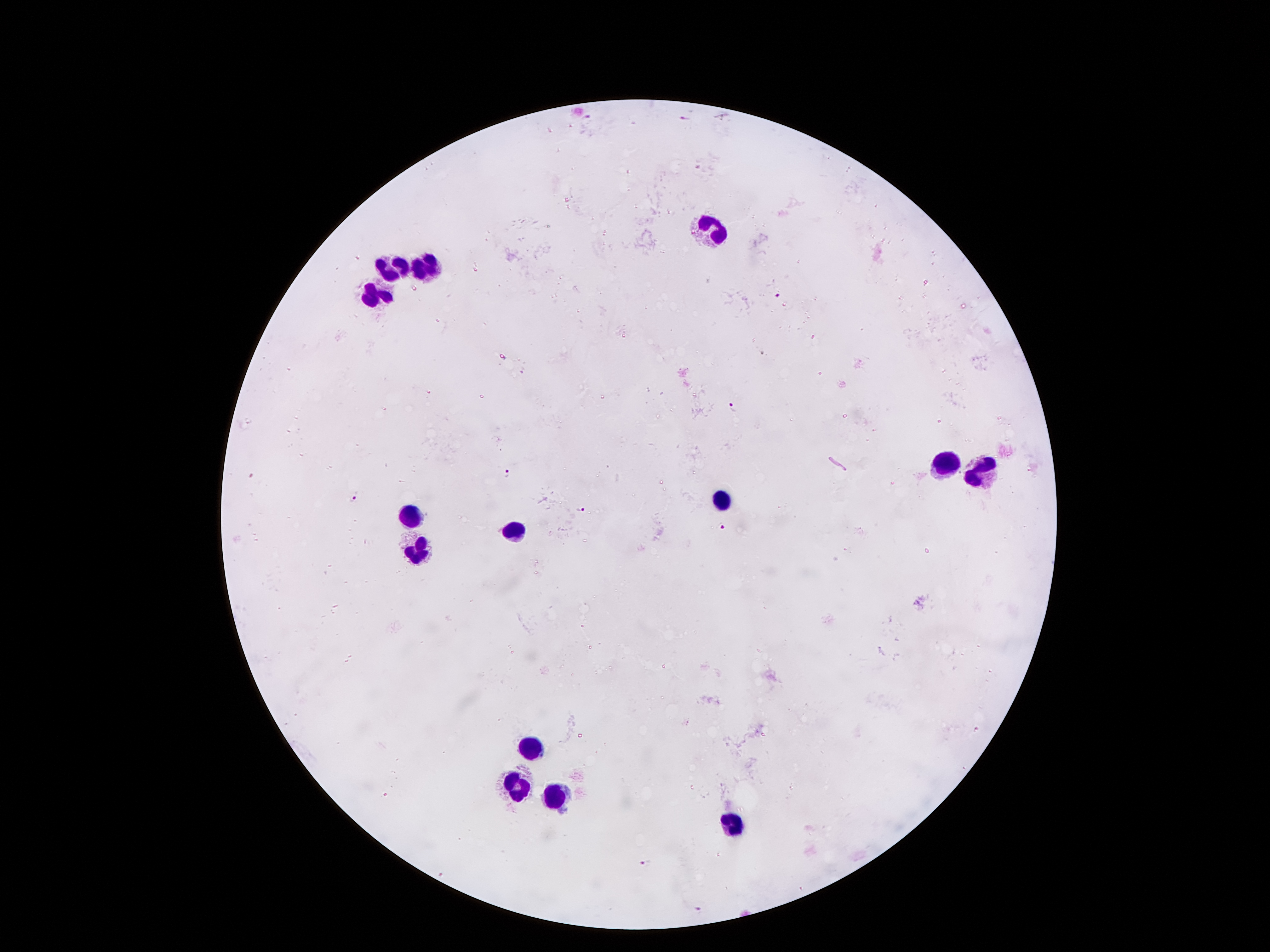
coordinate format = approximate centers as {x, y} in pixels
leukocyte locations = {711, 241}, {386, 267}, {428, 269}, {377, 298}, {944, 465}, {982, 473}, {720, 500}, {411, 519}, {512, 532}, {419, 550}, {535, 746}, {520, 787}, {552, 802}, {732, 825}
Plasmodium parasite locations = {587, 116}, {684, 120}, {778, 295}, {760, 354}, {733, 405}, {508, 472}, {354, 498}, {582, 511}, {724, 527}, {647, 863}, {697, 908}
magnification = 100x
field of view = one from this slide
preparation = thick peripheral-blood smear
capture = smartphone through the microscope eyepiece
stain = Giemsa
image size = 1270×952 pixels
patient malaria status = positive for Plasmodium falciparum